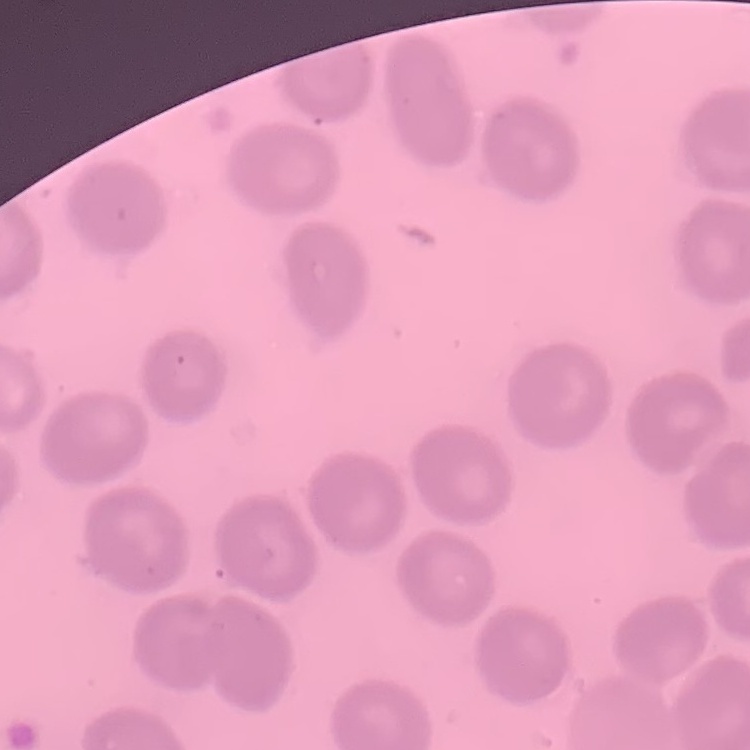
erythrocyte morphology = no rouleaux formation
stain = Field's or Giemsa
preparation = thin blood smear
image type = square crop of a larger photomicrograph